Outline every leukocyte.
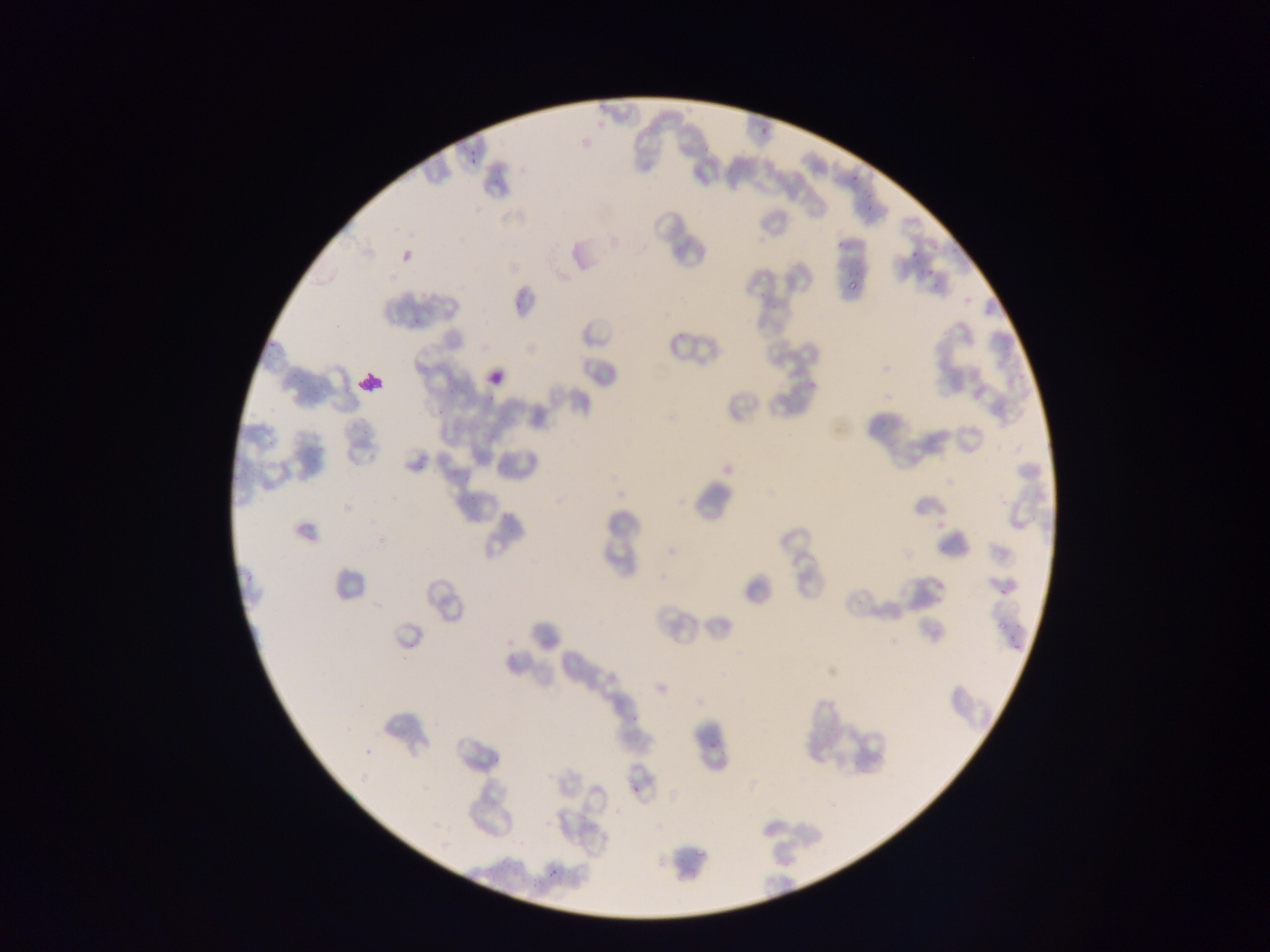

Approximate bounding boxes as [left, top, right, bottom] in pixels.
Leukocytes: [483, 362, 510, 392].
One object is labeled both Plasmodium parasite and leukocyte by the source: [356, 368, 383, 395].

image_size: 1270×952 pixels
capture: mobile-phone photograph through a microscope
preparation: thin blood film
country: Ghana
plasmodium_parasite_locations: 'approximate bounding boxes as [left, top, right, bottom] in pixels: [597, 102, 610, 114], [637, 127, 650, 138], [761, 127, 768, 137], [469, 158, 477, 167], [850, 175, 858, 184], [402, 250, 411, 262], [927, 268, 936, 277], [844, 276, 856, 293], [548, 870, 557, 879]'
field_of_view: single